Mark where Plasmodium parasites and white blood cells are.
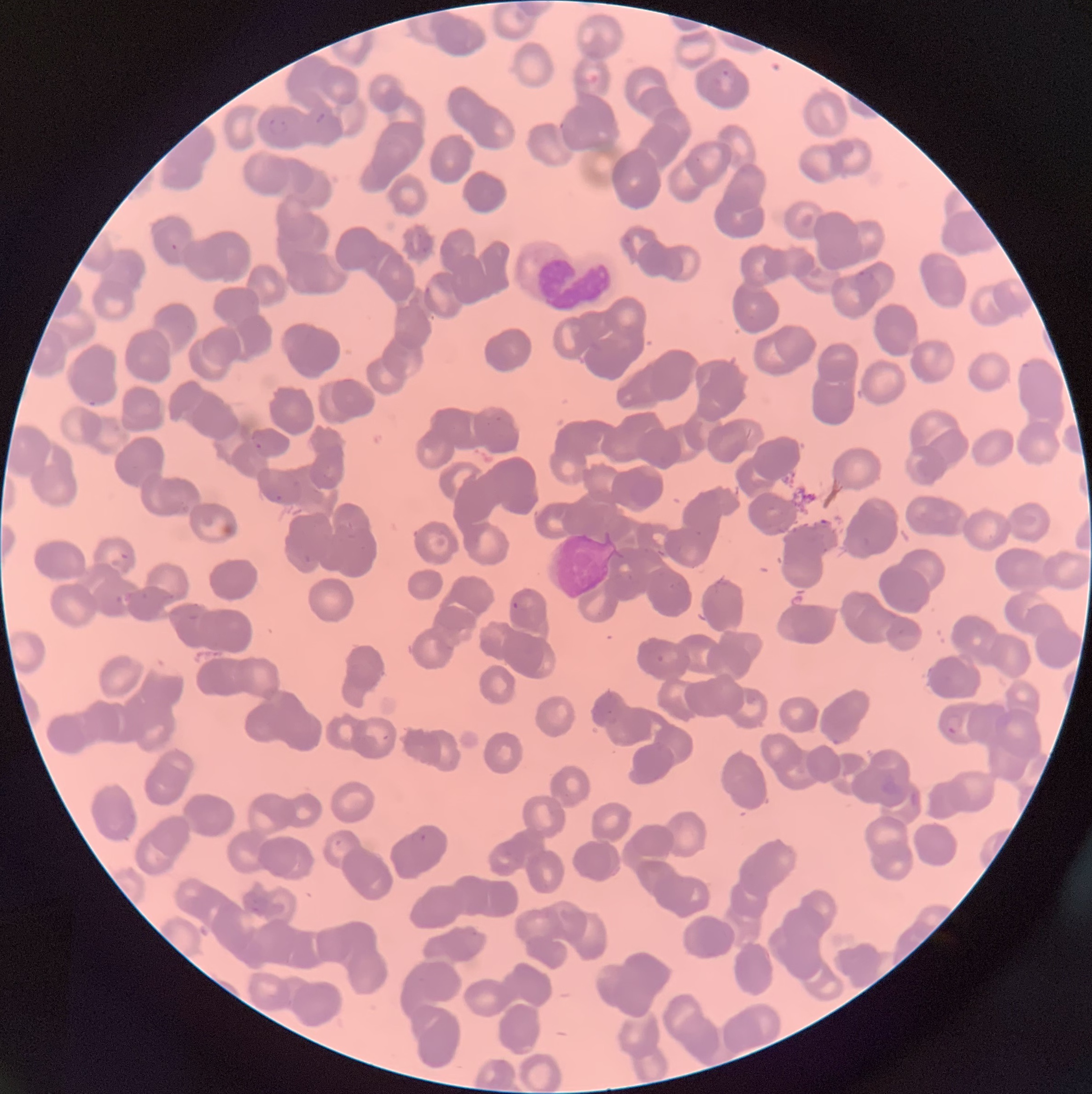
Approximate bounding boxes as [x1, y1, x2, y2] in pixels.
Plasmodium parasites: [712, 67, 732, 92], [313, 111, 326, 127], [263, 116, 289, 137], [169, 242, 179, 252], [855, 270, 875, 286], [424, 285, 433, 297], [254, 441, 262, 450], [262, 486, 282, 503], [511, 600, 520, 611], [655, 653, 665, 664], [606, 710, 620, 724], [944, 714, 962, 734], [832, 737, 842, 746], [410, 831, 427, 843].
White blood cells: [516, 244, 618, 311].

Summary:
  - Modality: optical microscopy
  - Preparation: thin blood film
  - Image size: 1092×1094 pixels
  - Red blood cell morphology: rouleaux formation